Outline each Plasmodium falciparum-infected red blood cell.
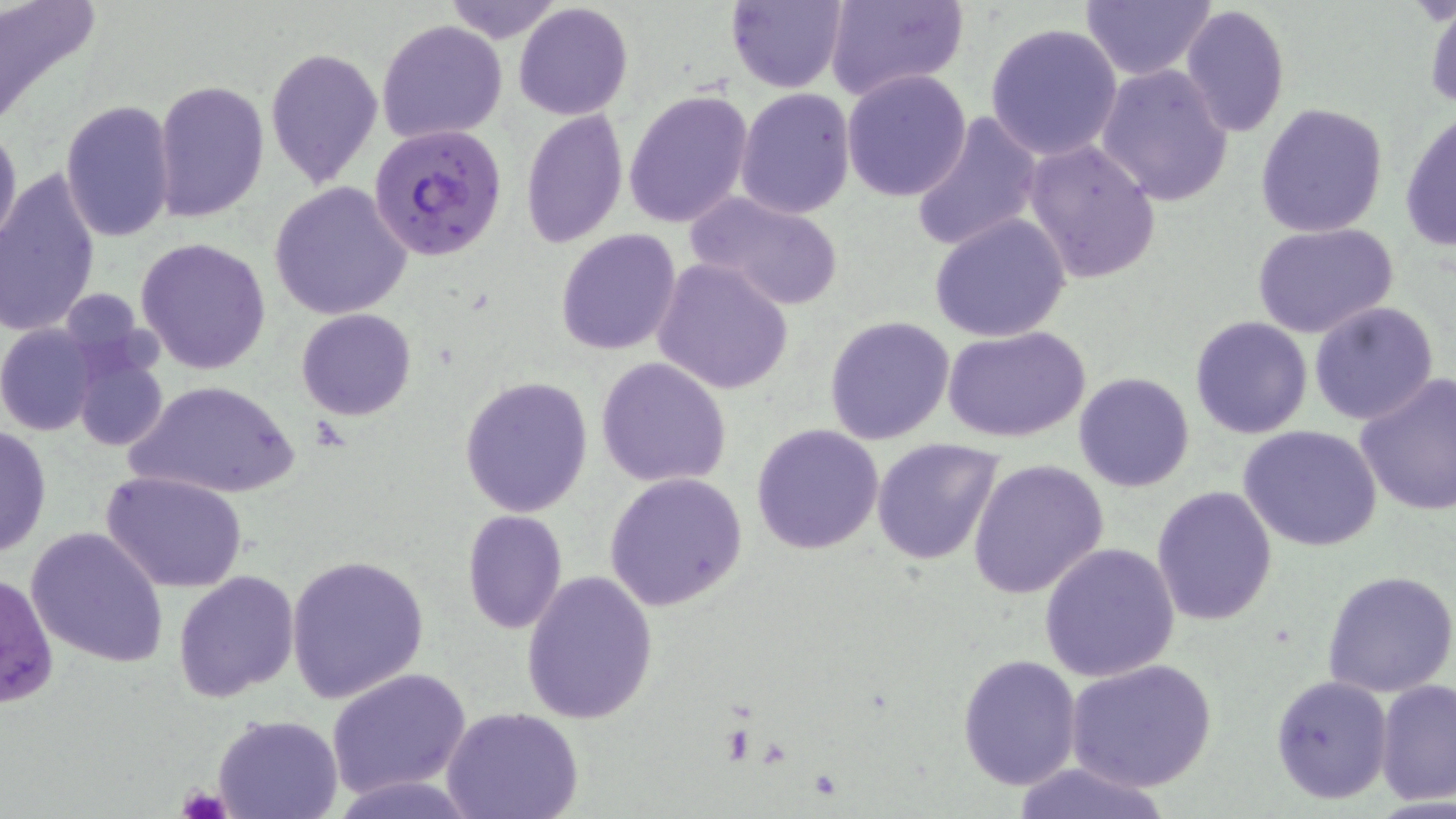
Approximate bounding boxes as (x1,y1)-(x2,y2) corner pairs in pixels.
Plasmodium falciparum-infected red blood cells: (371,124)-(508,263).

Summary:
  - Platelet locations: (177,785)-(233,819)
  - Uninfected red blood cell locations: (0,0)-(101,127), (441,0)-(567,43), (724,0)-(848,92), (823,0)-(968,101), (1080,1)-(1217,82), (513,2)-(633,120), (1179,3)-(1290,139), (1424,6)-(1456,110), (377,19)-(509,143), (985,24)-(1124,161), (264,45)-(383,190), (1096,64)-(1234,205), (842,69)-(972,201), (155,80)-(268,224), (735,87)-(855,217), (623,89)-(752,231), (59,101)-(176,242), (1255,102)-(1387,237), (520,110)-(629,248), (1399,110)-(1456,253), (909,111)-(1043,255), (0,119)-(22,254), (1023,138)-(1162,284), (0,169)-(100,340), (269,181)-(411,321), (684,189)-(847,311), (929,214)-(1071,342), (1251,222)-(1398,339), (555,227)-(682,357), (136,235)-(271,375), (653,257)-(794,395), (1307,301)-(1439,426), (296,308)-(416,420), (825,315)-(954,444), (1189,316)-(1314,439), (0,322)-(100,435), (944,326)-(1093,444), (73,344)-(170,454), (595,358)-(732,487), (1073,372)-(1194,492), (1354,372)-(1456,517), (460,377)-(592,516), (129,380)-(298,501), (752,423)-(884,555), (1238,424)-(1384,552), (0,425)-(50,557), (871,438)-(1005,567), (967,458)-(1109,599), (101,470)-(246,592), (606,472)-(748,612), (1151,486)-(1278,628), (461,509)-(566,634), (26,526)-(168,669), (1038,541)-(1181,683), (285,553)-(428,702), (1323,567)-(1456,698), (1,569)-(58,708), (174,569)-(300,704), (520,572)-(657,724), (956,652)-(1083,791), (1068,659)-(1216,793), (326,667)-(472,798), (1270,674)-(1393,804), (1374,679)-(1456,805), (441,707)-(584,819), (212,714)-(342,819), (1007,761)-(1177,819)
  - Slide-level diagnosis: Plasmodium falciparum
  - Magnification: 1000x
  - Field of view: single
  - Preparation: thin blood film
  - Image size: 1456×819 pixels
  - Modality: optical microscopy
  - Stain: May-Grünwald-Giemsa